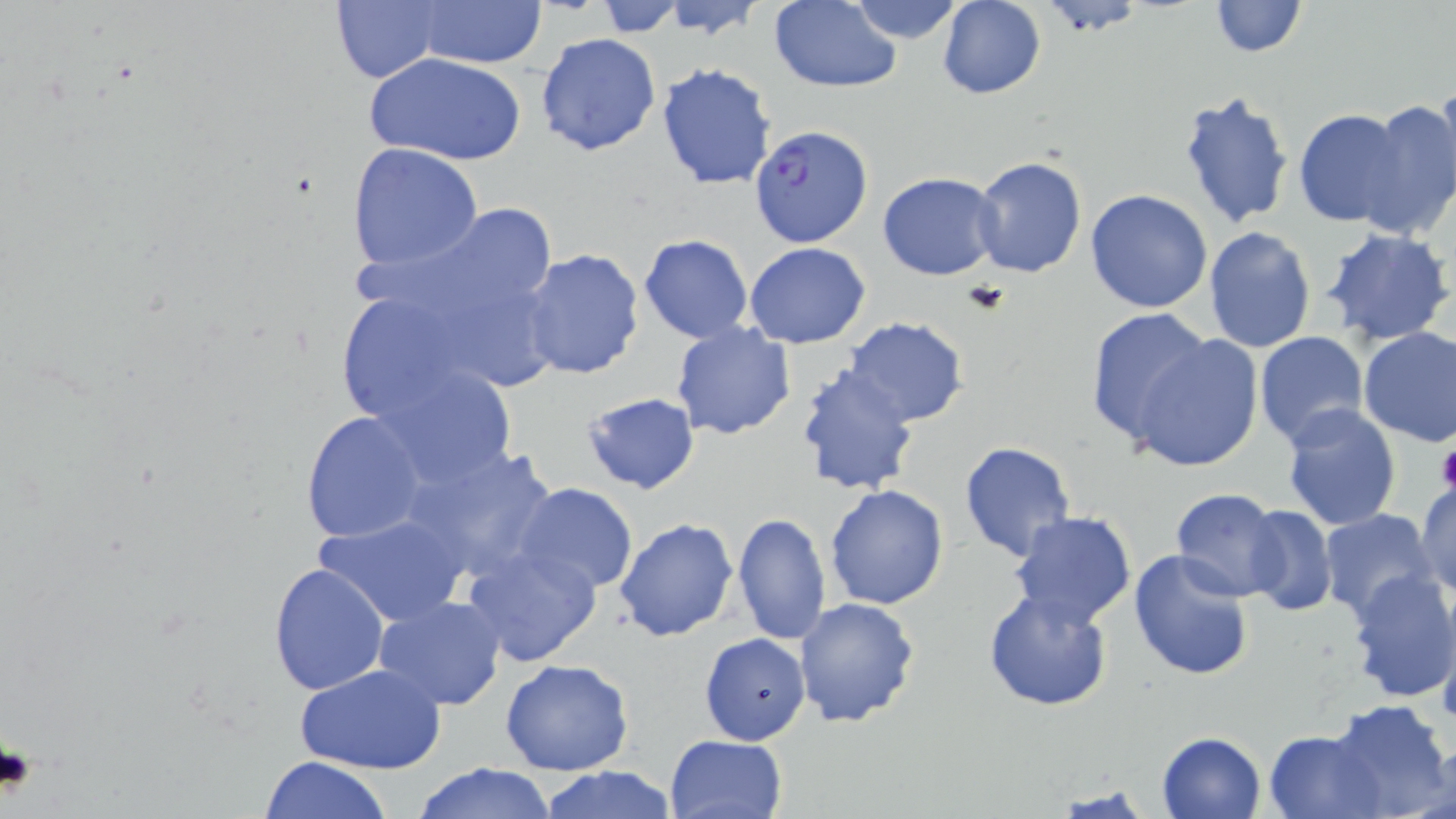

Approximate bounding boxes as [x1, y1, x2, y2] in pixels. Platelet locations: [1436, 440, 1456, 497], [0, 739, 37, 797]. Uninfected red blood cell locations: [659, 0, 768, 43], [1208, 0, 1307, 57], [591, 1, 688, 35], [846, 1, 968, 44], [937, 1, 1047, 100], [411, 2, 549, 69], [768, 2, 902, 91], [329, 3, 445, 85], [535, 32, 661, 157], [367, 53, 525, 166], [656, 61, 777, 191], [1434, 78, 1456, 207], [1176, 90, 1293, 230], [1360, 97, 1456, 235], [1292, 109, 1414, 228], [347, 143, 484, 272], [971, 156, 1087, 278], [878, 172, 1002, 279], [1086, 188, 1215, 314], [347, 205, 571, 331], [1204, 226, 1317, 354], [1321, 227, 1453, 346], [639, 234, 754, 343], [744, 242, 871, 347], [518, 247, 646, 381], [328, 284, 494, 429], [1085, 307, 1216, 448], [842, 316, 969, 426], [671, 323, 798, 441], [1359, 326, 1456, 448], [1124, 331, 1266, 471], [1254, 331, 1370, 449], [373, 364, 521, 489], [796, 370, 920, 495], [581, 389, 701, 496], [1281, 403, 1401, 531], [300, 410, 428, 545], [957, 441, 1076, 562], [401, 442, 559, 583], [1414, 479, 1456, 600], [512, 483, 640, 596], [824, 484, 949, 610], [1170, 489, 1290, 601], [1241, 505, 1338, 617], [1317, 509, 1440, 624], [1007, 510, 1138, 629], [731, 511, 831, 649], [315, 512, 469, 627], [615, 517, 739, 642], [462, 543, 602, 668], [1127, 549, 1256, 682], [269, 563, 390, 696], [1343, 570, 1456, 704], [982, 587, 1115, 713], [374, 596, 506, 710], [793, 597, 920, 728], [1436, 600, 1456, 730], [699, 632, 810, 745], [500, 657, 635, 776], [296, 662, 447, 775], [1328, 698, 1453, 818], [1264, 728, 1381, 818], [1157, 730, 1267, 819], [665, 734, 788, 819], [260, 756, 393, 819], [411, 762, 558, 818], [535, 766, 678, 819]. Plasmodium falciparum-infected red blood cell locations: [749, 125, 873, 249]. Slide-level diagnosis: Plasmodium falciparum. Image is 1456×819 pixels. Thin blood film. May-Grünwald-Giemsa-stained preparation. One field of a larger specimen. Light microscopy. 1000x magnification.